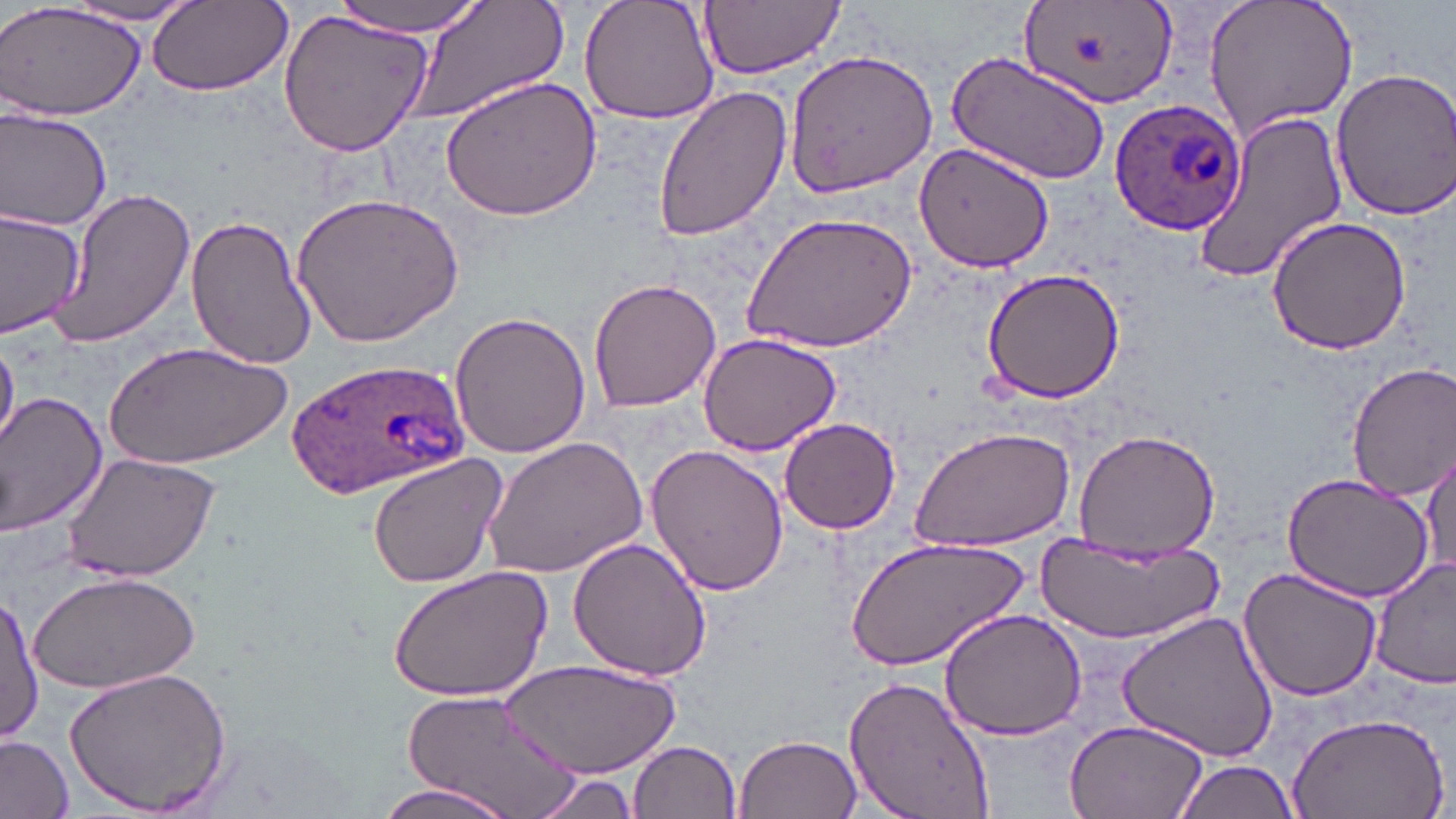

Approximate bounding boxes as [x1, y1, x2, y2] in pixels. Plasmodium ovale-infected red blood cell locations: [1109, 100, 1245, 239], [283, 355, 472, 498]. Uninfected red blood cell locations: [335, 0, 487, 34], [405, 0, 569, 123], [578, 0, 723, 124], [698, 0, 844, 79], [1202, 0, 1359, 141], [147, 1, 294, 98], [1016, 1, 1181, 113], [0, 2, 144, 121], [60, 2, 205, 27], [279, 8, 434, 160], [784, 49, 939, 195], [944, 51, 1112, 185], [1328, 65, 1456, 222], [438, 73, 603, 222], [652, 82, 793, 242], [0, 105, 113, 233], [1190, 110, 1349, 285], [918, 141, 1058, 272], [43, 185, 197, 348], [291, 188, 463, 347], [0, 207, 86, 337], [741, 212, 916, 355], [184, 214, 315, 368], [1265, 215, 1412, 358], [979, 269, 1125, 405], [589, 276, 723, 413], [449, 309, 590, 459], [696, 331, 843, 459], [0, 337, 19, 452], [104, 339, 293, 467], [1346, 362, 1456, 500], [0, 391, 108, 537], [778, 418, 903, 535], [910, 427, 1077, 554], [1072, 428, 1220, 557], [481, 436, 644, 580], [1422, 443, 1454, 582], [644, 445, 790, 598], [61, 451, 220, 585], [366, 454, 507, 589], [1280, 473, 1433, 604], [850, 534, 1027, 672], [1033, 534, 1223, 642], [568, 536, 714, 683], [1368, 558, 1456, 692], [387, 565, 553, 703], [1238, 567, 1383, 702], [30, 569, 202, 695], [1, 590, 41, 747], [938, 606, 1089, 740], [1119, 609, 1279, 764], [503, 657, 676, 780], [67, 666, 233, 816], [843, 673, 999, 819], [397, 687, 589, 817], [1286, 707, 1450, 819], [1061, 716, 1210, 819], [735, 732, 862, 819], [0, 733, 74, 818], [630, 740, 742, 819], [1172, 757, 1301, 819], [528, 769, 649, 819], [368, 779, 521, 819]. Slide-level diagnosis: Plasmodium ovale. May-Grünwald-Giemsa stain. Optical microscopy. One field of a larger specimen. 1000x magnification. Image is 1456×819 pixels. Thin blood film.